Evaluate for Plasmodium parasites.
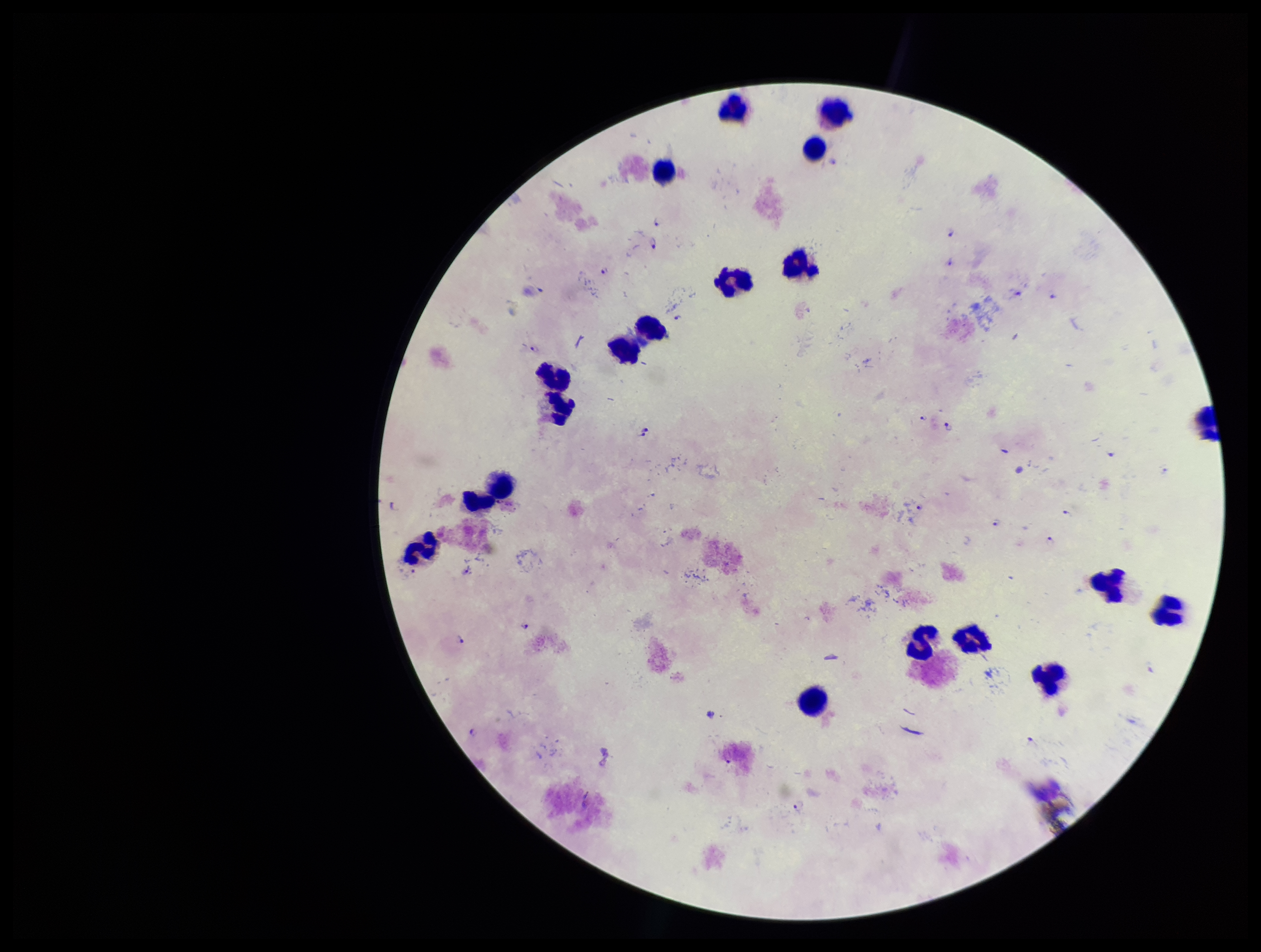
Detected.

Summary:
  - Leukocyte count: 17
  - Preparation: thick
  - Patient malaria status: infected
  - Capture: smartphone photograph through the microscope eyepiece
  - Species reported for this patient: Plasmodium falciparum
  - Image size: 1261×952 pixels
  - Field of view: single
  - Stain: Giemsa
  - Parasite count: 23